State which parasite is depicted.
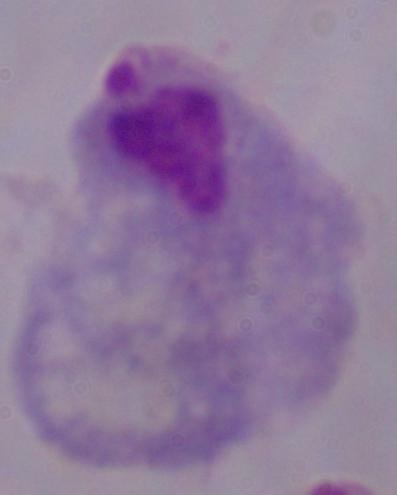

This is a trichomonad.

Summary:
  - Modality: photomicrograph
  - Magnification: 1000x